Report the malaria status of this cell.
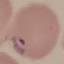

Parasitized.

Summary:
  - Preparation: thin blood smear
  - Capture: smartphone camera at the microscope eyepiece
  - Image type: cell patch, automatically extracted from a larger field of view and resized to 64 × 64 pixels
  - Stain: Giemsa